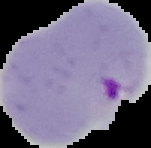

preparation = thin blood film
image size = 151×148 pixels
image type = segmented cell region on a black background
result = malaria parasites detected